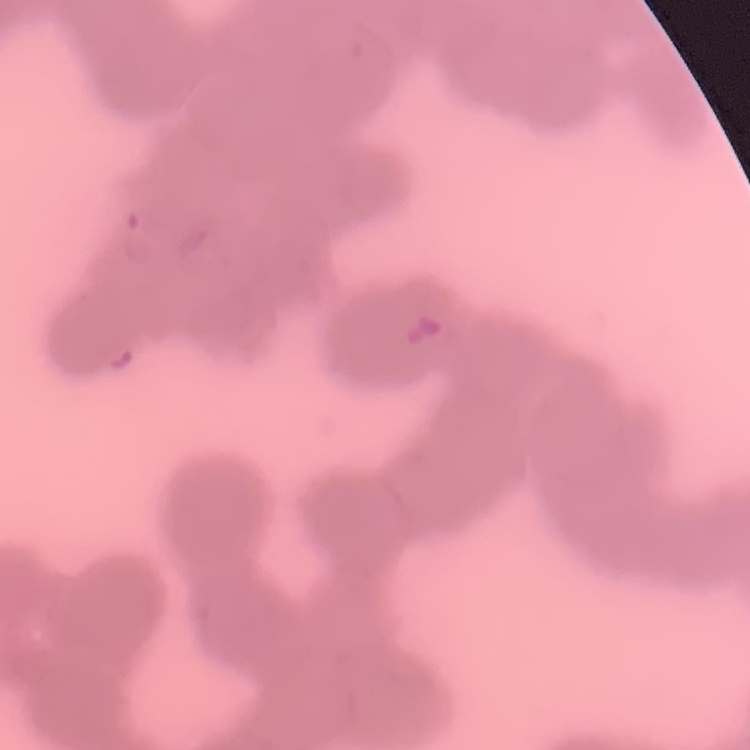
Summary:
  - Erythrocyte morphology: rouleaux formation
  - Image type: one tile cut from a larger photomicrograph
  - Preparation: thin blood smear
  - Stain: Field's or Giemsa